State which parasite is depicted.
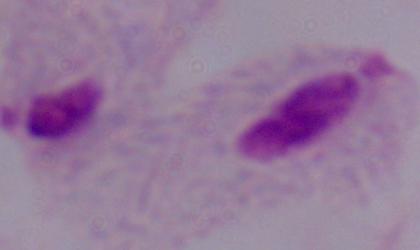
This is a trichomonad.

Photomicrograph. Captured at 1000x magnification.